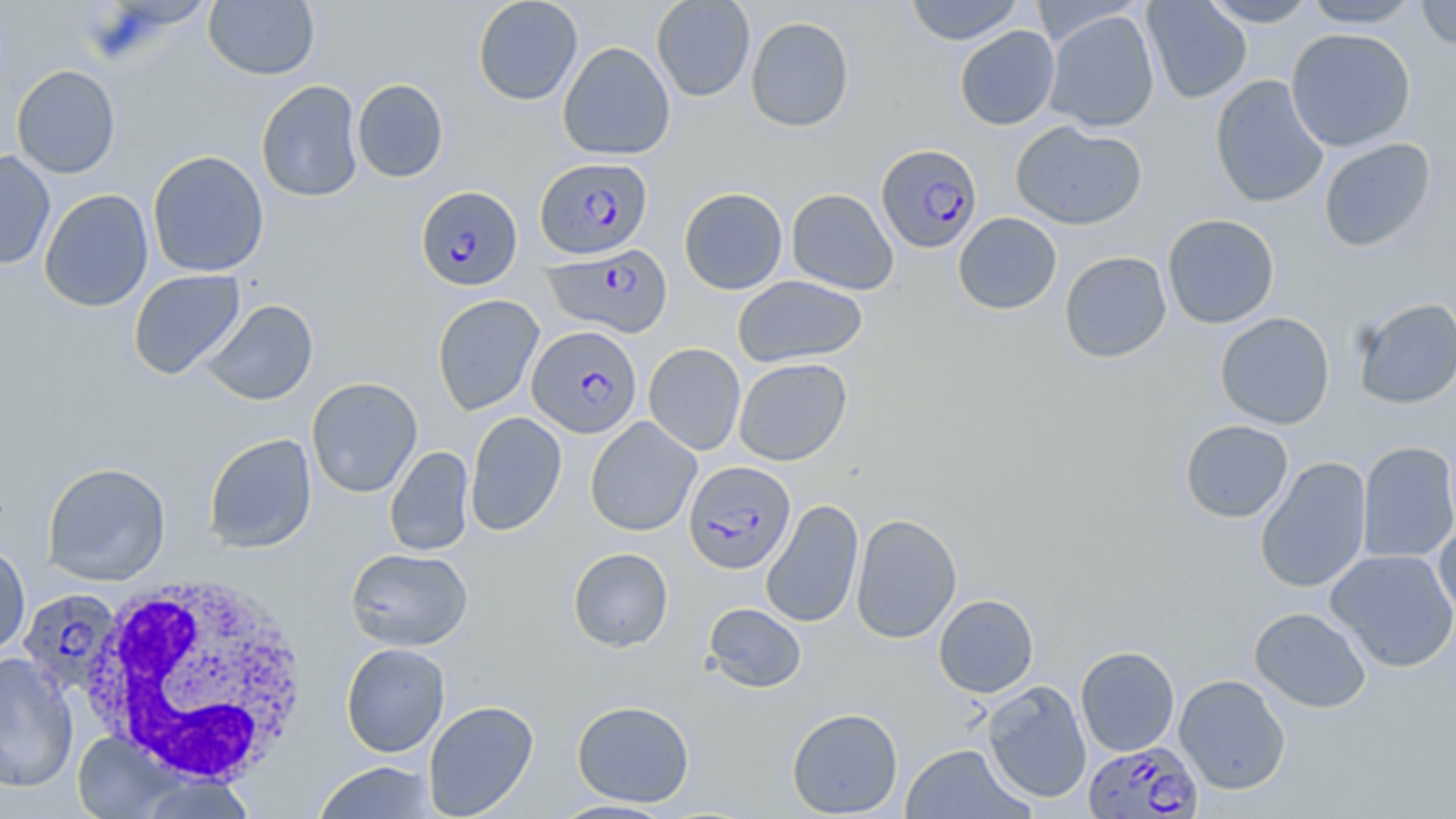

Summary:
  - Coordinate format: approximate bounding boxes as (x1,y1)-(x2,y2) corner pairs in pixels
  - White blood cell locations: (82,573)-(312,785)
  - Uninfected red blood cell locations: (204,0)-(319,80), (472,0)-(583,106), (651,0)-(755,102), (904,0)-(1024,45), (1142,0)-(1252,103), (1201,0)-(1320,27), (1302,0)-(1422,29), (1416,0)-(1456,50), (1044,9)-(1159,133), (745,15)-(855,132), (954,25)-(1060,130), (1286,28)-(1417,152), (558,41)-(675,161), (11,65)-(121,178), (1209,74)-(1329,208), (352,78)-(449,182), (256,80)-(364,202), (1010,121)-(1147,230), (1319,138)-(1436,252), (0,150)-(56,270), (147,150)-(269,277), (678,187)-(788,295), (786,188)-(899,295), (39,189)-(154,313), (953,212)-(1062,315), (1162,213)-(1280,329), (1059,251)-(1172,363), (128,269)-(246,380), (733,275)-(867,368), (432,294)-(544,414), (1352,297)-(1456,409), (198,299)-(318,405), (1215,312)-(1335,429), (644,343)-(746,455), (734,358)-(852,466), (306,377)-(423,498), (465,411)-(567,536), (586,416)-(702,536), (1180,420)-(1293,523), (203,433)-(317,554), (1357,441)-(1456,563), (384,445)-(474,556), (1255,456)-(1372,593), (42,462)-(171,586), (761,498)-(864,629), (850,513)-(962,644), (1433,522)-(1456,626), (0,541)-(30,656), (345,547)-(473,651), (568,547)-(673,652), (1325,548)-(1456,672), (933,594)-(1039,698), (702,602)-(807,693), (1249,607)-(1372,713), (341,642)-(450,757), (1075,646)-(1180,756), (0,652)-(79,794), (1174,674)-(1291,794), (982,679)-(1092,803), (423,700)-(539,818), (571,700)-(695,807), (787,707)-(903,817), (73,732)-(174,818), (900,743)-(1033,818), (312,760)-(440,818), (137,774)-(259,819), (548,799)-(678,818)
  - Plasmodium falciparum-infected red blood cell locations: (876,144)-(983,254), (535,156)-(652,259), (416,186)-(522,291), (544,244)-(673,339), (527,325)-(642,438), (684,461)-(795,574), (17,588)-(123,698), (1083,739)-(1203,819)
  - Slide-level diagnosis: Plasmodium falciparum
  - Preparation: thin blood film
  - Image size: 1456×819 pixels
  - Stain: May-Grünwald-Giemsa
  - Field of view: single
  - Magnification: 1000x
  - Modality: optical microscopy